Classify this cell by malaria status.
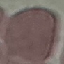
It is uninfected.

image type = cell patch, automatically extracted from a larger field of view and resized to 64 × 64 pixels
preparation = thin smear
stain = Giemsa
capture = smartphone through the microscope eyepiece